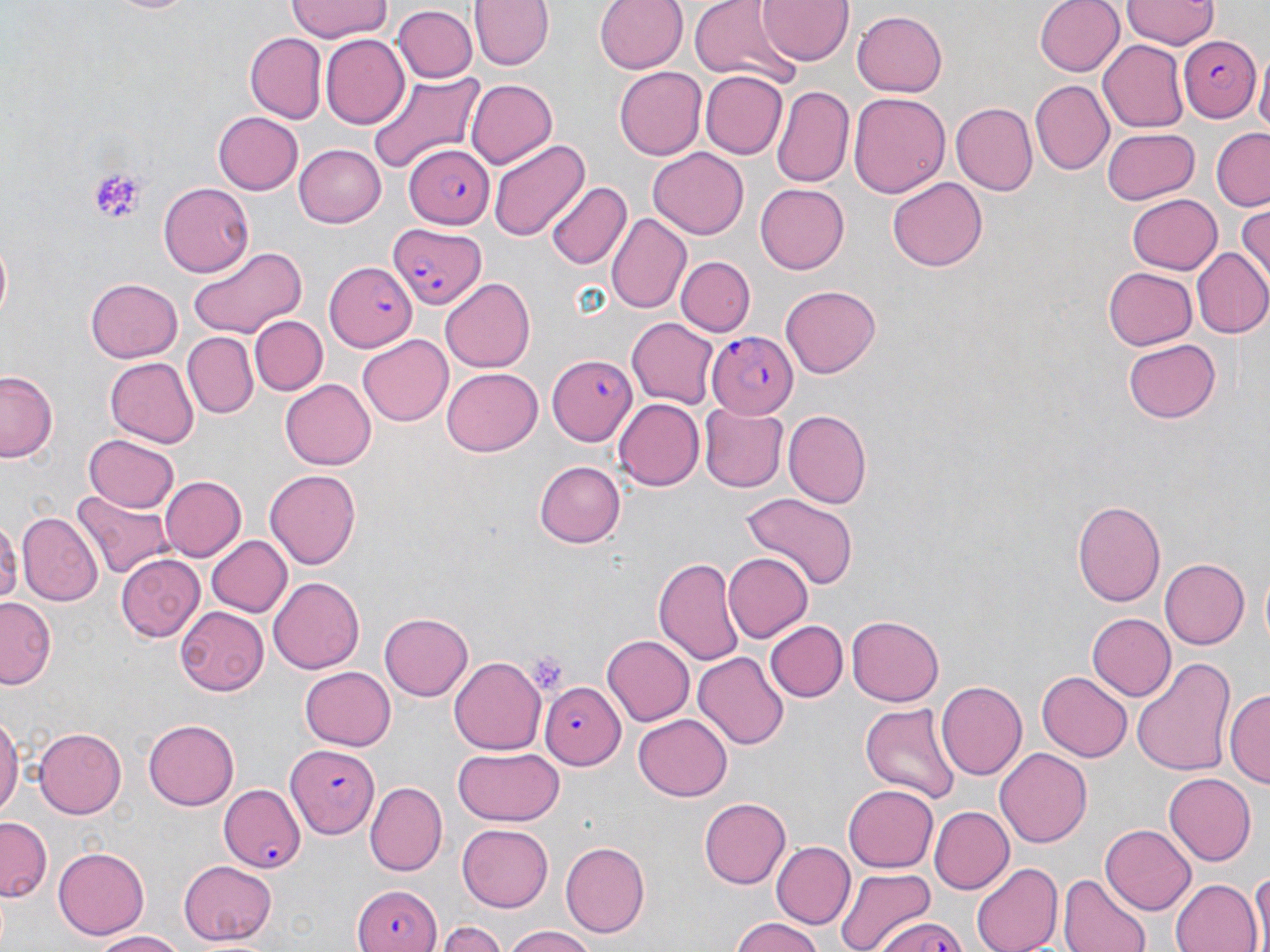
Summary:
  - Coordinate format: approximate bounding boxes as (x1,y1)-(x2,y2) corner pairs in pixels
  - Uninfected red blood cell locations: (101,0)-(201,16), (288,0)-(392,42), (472,0)-(553,71), (595,0)-(687,74), (690,0)-(792,82), (759,0)-(852,64), (1033,0)-(1124,77), (1121,0)-(1217,47), (392,5)-(478,84), (855,10)-(948,96), (245,32)-(326,122), (320,36)-(409,126), (1100,38)-(1190,132), (1255,62)-(1270,143), (613,64)-(705,157), (368,71)-(486,174), (700,71)-(784,159), (464,79)-(558,172), (1028,79)-(1113,172), (774,85)-(852,186), (848,91)-(948,197), (950,104)-(1036,196), (213,111)-(303,194), (1114,126)-(1209,264), (1102,129)-(1198,204), (1211,129)-(1270,210), (487,137)-(589,243), (294,144)-(385,227), (648,147)-(749,237), (888,178)-(988,272), (161,181)-(255,277), (546,182)-(631,270), (755,183)-(850,273), (1126,193)-(1222,274), (1236,205)-(1270,287), (606,214)-(691,314), (188,246)-(308,337), (1192,247)-(1270,339), (677,256)-(754,337), (1103,267)-(1197,350), (85,278)-(183,362), (440,278)-(534,373), (781,283)-(881,375), (251,316)-(326,395), (627,319)-(719,407), (181,331)-(256,418), (358,332)-(452,423), (1121,338)-(1221,425), (104,357)-(198,447), (442,368)-(544,456), (1,369)-(61,463), (279,379)-(375,470), (613,398)-(703,488), (701,405)-(787,492), (784,409)-(871,506), (84,433)-(179,513), (533,461)-(624,548), (264,469)-(361,571), (159,477)-(245,562), (72,489)-(173,580), (737,491)-(860,588), (1072,497)-(1166,608), (16,512)-(100,605), (0,517)-(17,611), (206,536)-(290,617), (723,552)-(813,641), (116,554)-(205,643), (1158,555)-(1253,648), (656,556)-(745,665), (269,576)-(367,673), (0,598)-(54,686), (176,606)-(270,696), (380,611)-(473,701), (1088,613)-(1174,703), (847,615)-(944,706), (762,621)-(846,703), (601,637)-(693,726), (695,651)-(788,748), (450,658)-(545,752), (1130,658)-(1233,779), (299,667)-(396,750), (1037,672)-(1132,761), (935,681)-(1026,779), (1228,688)-(1269,791), (859,702)-(959,804), (0,712)-(21,818), (633,714)-(733,801), (143,719)-(240,810), (35,726)-(127,818), (994,747)-(1091,847), (454,748)-(565,826), (1164,773)-(1256,866), (365,780)-(447,873), (844,782)-(937,873), (699,797)-(791,888), (932,805)-(1013,895), (1,816)-(53,902), (1102,823)-(1196,915), (457,824)-(554,910), (773,841)-(854,927), (559,842)-(651,939), (52,846)-(149,939), (177,859)-(278,942), (972,862)-(1061,952), (834,866)-(936,952), (1251,866)-(1269,952), (1059,874)-(1153,952), (1170,878)-(1261,952), (729,917)-(825,952), (438,923)-(508,952), (502,925)-(599,952), (88,930)-(188,950)
  - Platelet locations: (88,170)-(145,225), (524,651)-(571,694)
  - Plasmodium falciparum-infected red blood cell locations: (1176,36)-(1260,120), (405,145)-(495,227), (390,220)-(485,311), (325,264)-(418,353), (708,331)-(799,418), (548,355)-(640,442), (539,682)-(623,769), (286,746)-(379,837), (216,777)-(306,873), (354,882)-(440,952), (870,917)-(971,952)
  - Slide-level diagnosis: Plasmodium falciparum
  - Stain: May-Grünwald-Giemsa
  - Field of view: one of a larger specimen
  - Modality: optical microscopy
  - Magnification: 1000x
  - Image size: 1270×952 pixels
  - Preparation: thin blood film